Report the malaria status.
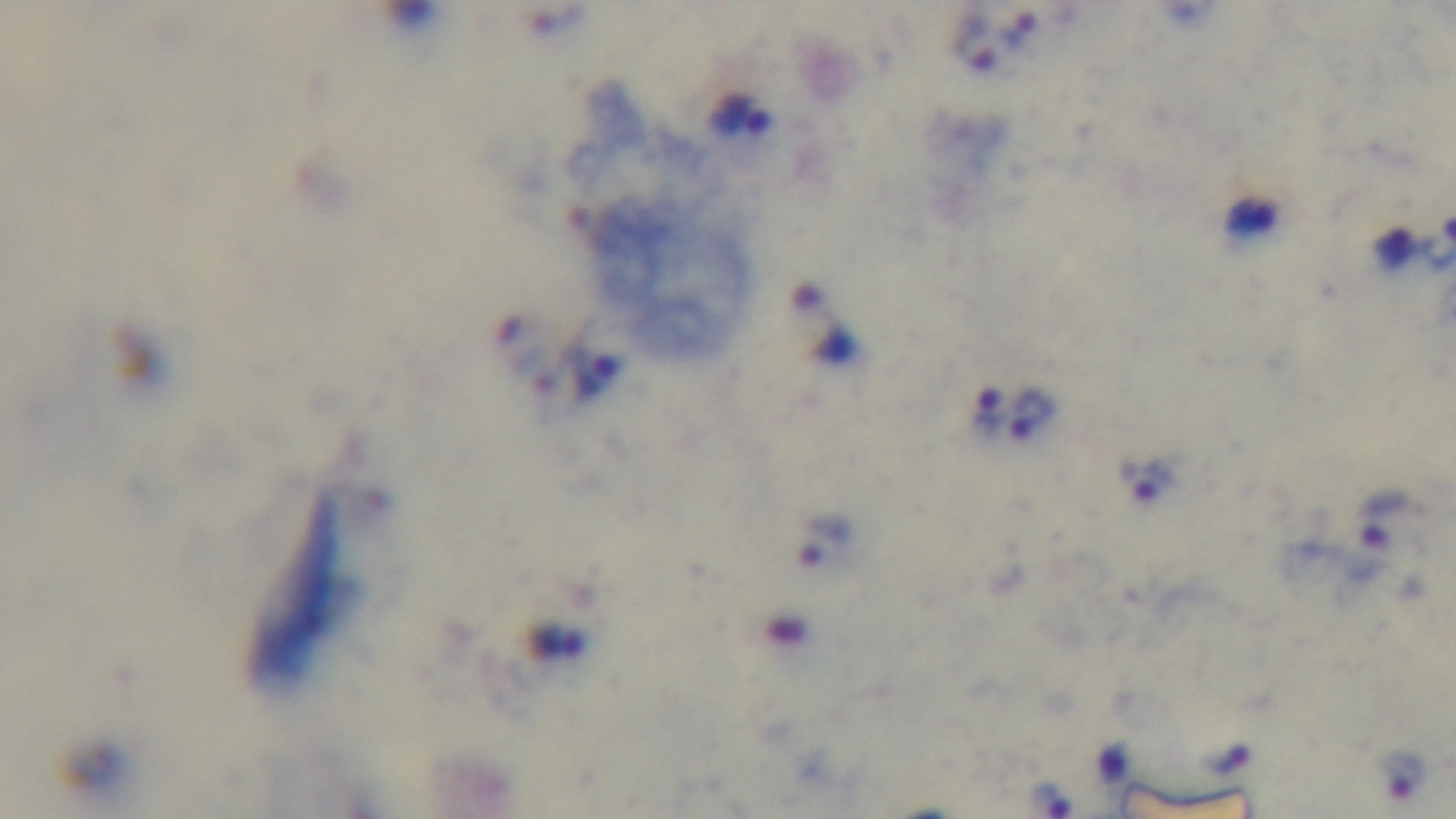

It is infected.

preparation = thick blood film
modality = light microscopy
stain = Giemsa
objective = 100x oil immersion
capture = mounted 4K digital camera
field of view = one from the slide